Describe the morphology of the red blood cells.
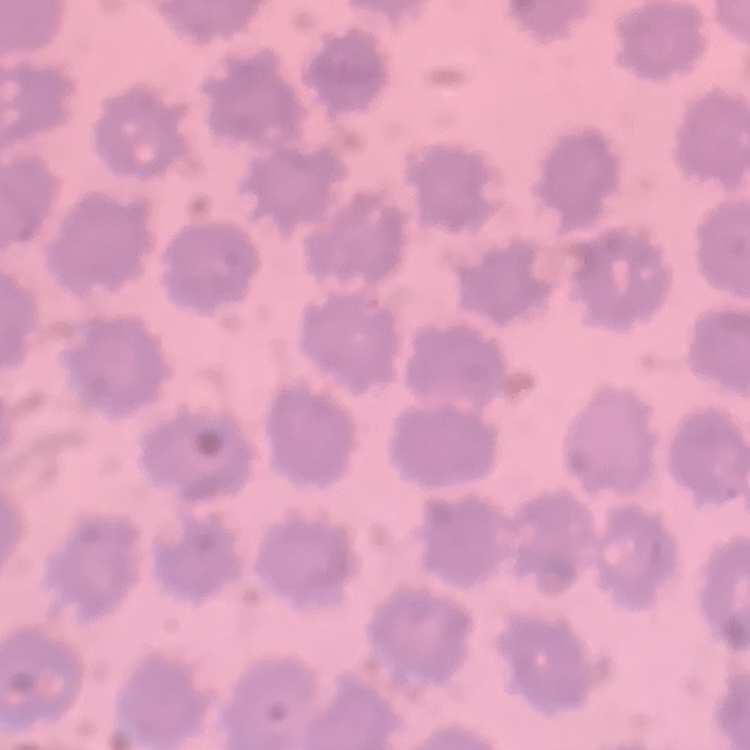

They show no rouleaux formation.

stain: Field's or Giemsa
image_type: one tile cut from a larger photomicrograph
preparation: thin peripheral smear